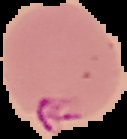

malaria_status: parasitized
image_size: 127×139 pixels
preparation: thin blood smear
image_type: cell region segmented out of the field of view; surrounding area masked to black